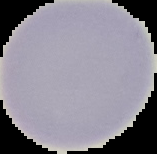

result: no Plasmodium parasites detected
image_type: segmented cell region on a black background
preparation: thin blood smear
image_size: 157×154 pixels